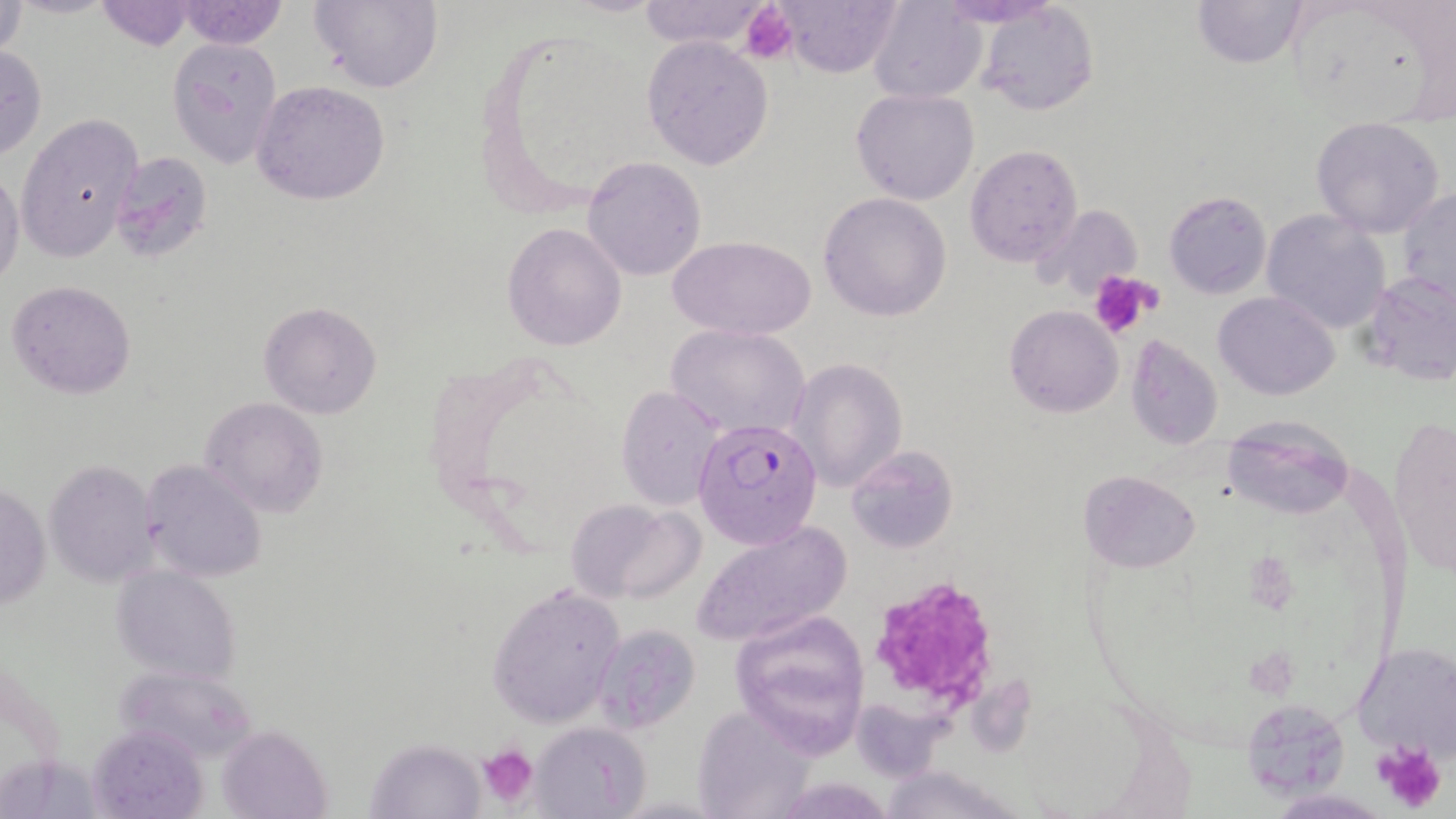
{
  "slide_level_diagnosis": "Plasmodium falciparum",
  "platelet_locations": "approximate bounding boxes as [x1, y1, x2, y2] in pixels: [741, 3, 798, 63], [1089, 270, 1161, 339], [874, 579, 1000, 704], [1373, 740, 1448, 816], [479, 745, 538, 810]",
  "magnification": "1000x",
  "preparation": "thin blood film",
  "field_of_view": "single",
  "stain": "May-Grünwald-Giemsa",
  "uninfected_red_blood_cell_locations": "approximate bounding boxes as [x1, y1, x2, y2] in pixels: [175, 0, 287, 49], [310, 0, 442, 93], [635, 0, 770, 51], [767, 0, 905, 76], [1191, 0, 1310, 68], [94, 1, 199, 50], [870, 1, 988, 103], [1, 2, 28, 63], [975, 3, 1099, 117], [167, 36, 284, 168], [643, 36, 772, 171], [0, 44, 48, 162], [251, 80, 390, 205], [852, 88, 979, 206], [16, 114, 143, 262], [1310, 116, 1446, 238], [965, 142, 1085, 270], [109, 150, 215, 262], [582, 157, 707, 281], [0, 163, 25, 294], [1398, 185, 1456, 313], [1164, 191, 1270, 298], [818, 192, 951, 320], [1261, 210, 1390, 335], [502, 222, 627, 352], [671, 236, 813, 341], [1358, 270, 1455, 385], [7, 279, 136, 400], [1214, 291, 1340, 400], [259, 301, 383, 418], [1004, 304, 1124, 417], [667, 324, 810, 440], [1125, 335, 1223, 450], [793, 358, 904, 490], [616, 385, 726, 510], [199, 397, 328, 519], [1224, 416, 1355, 519], [1387, 416, 1455, 576], [845, 445, 958, 555], [141, 459, 268, 582], [45, 461, 158, 588], [1079, 469, 1200, 572], [1, 479, 49, 612], [564, 498, 699, 602], [694, 519, 850, 649], [111, 565, 242, 682], [487, 582, 626, 729], [736, 603, 882, 753], [589, 623, 700, 732], [1352, 642, 1456, 760], [1239, 699, 1351, 800], [692, 705, 816, 817], [530, 721, 650, 817], [90, 724, 209, 819], [216, 727, 332, 819], [367, 739, 482, 816], [879, 766, 1023, 819]",
  "modality": "light microscopy",
  "plasmodium_falciparum_infected_red_blood_cell_locations": "approximate bounding boxes as [x1, y1, x2, y2] in pixels: [694, 419, 822, 548]",
  "image_size": "1456×819 pixels"
}